Identify the blood parasite species.
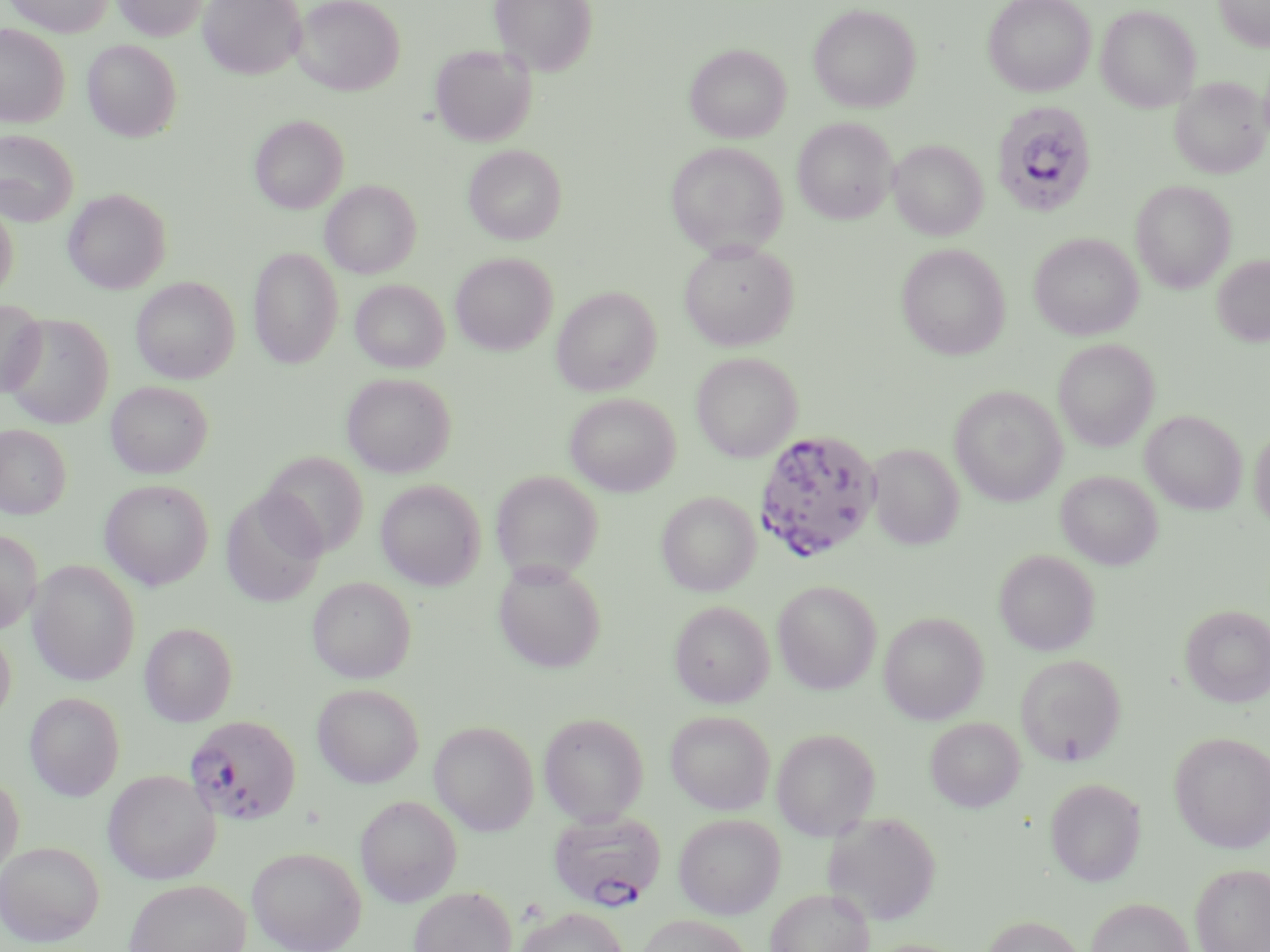
Plasmodium falciparum.

Summary:
  - Coordinate format: approximate bounding boxes as (x1,y1)-(x2,y2) corner pairs in pixels
  - Plasmodium falciparum-infected red blood cell locations: (991,100)-(1097,217), (753,430)-(882,563), (185,714)-(302,826), (548,810)-(666,911)
  - Uninfected red blood cell locations: (4,0)-(114,36), (112,0)-(207,41), (198,0)-(305,79), (293,0)-(404,96), (489,0)-(597,75), (983,0)-(1095,96), (1214,0)-(1270,51), (809,4)-(921,113), (1096,5)-(1201,112), (0,24)-(69,127), (83,39)-(182,142), (430,44)-(537,147), (686,44)-(790,143), (1169,77)-(1268,179), (249,115)-(348,213), (793,117)-(897,224), (0,129)-(79,225), (889,139)-(988,240), (665,142)-(788,258), (464,145)-(566,244), (321,180)-(421,278), (1131,180)-(1236,293), (63,187)-(172,294), (0,199)-(19,299), (1029,232)-(1144,340), (679,241)-(799,351), (896,244)-(1010,360), (248,247)-(343,369), (451,253)-(557,355), (1212,255)-(1270,346), (131,277)-(239,384), (350,279)-(449,373), (551,287)-(662,396), (0,298)-(47,397), (2,313)-(113,429), (1053,339)-(1159,451), (691,352)-(802,462), (341,372)-(456,477), (105,381)-(212,478), (950,386)-(1067,506), (565,393)-(680,496), (1141,410)-(1247,514), (0,424)-(71,518), (1249,424)-(1270,532), (868,443)-(964,550), (261,451)-(368,557), (491,469)-(604,582), (1056,470)-(1162,570), (99,479)-(214,590), (375,479)-(486,590), (221,490)-(327,608), (657,491)-(760,596), (0,528)-(42,633), (994,549)-(1099,656), (28,560)-(141,686), (493,560)-(607,674), (307,577)-(416,683), (772,580)-(882,694), (669,601)-(774,708), (1180,604)-(1270,707), (879,612)-(988,724), (139,622)-(237,726), (0,624)-(16,724), (1015,654)-(1127,766), (312,683)-(423,788), (24,692)-(126,801), (666,710)-(775,814), (538,712)-(649,825), (926,717)-(1025,812), (429,721)-(540,835), (771,728)-(881,840), (1169,731)-(1270,853), (103,770)-(220,885), (0,771)-(24,877), (1045,777)-(1146,886), (355,795)-(462,907), (823,811)-(942,925), (674,814)-(785,919), (0,841)-(104,947), (246,846)-(367,952), (1191,863)-(1270,952), (123,878)-(251,952), (409,886)-(517,952), (766,888)-(874,952), (1085,897)-(1194,952), (516,906)-(629,952), (636,914)-(752,952), (981,914)-(1086,952)
  - Magnification: 1000x
  - Stain: May-Grünwald-Giemsa
  - Modality: light microscopy
  - Preparation: thin blood film
  - Field of view: single
  - Image size: 1270×952 pixels